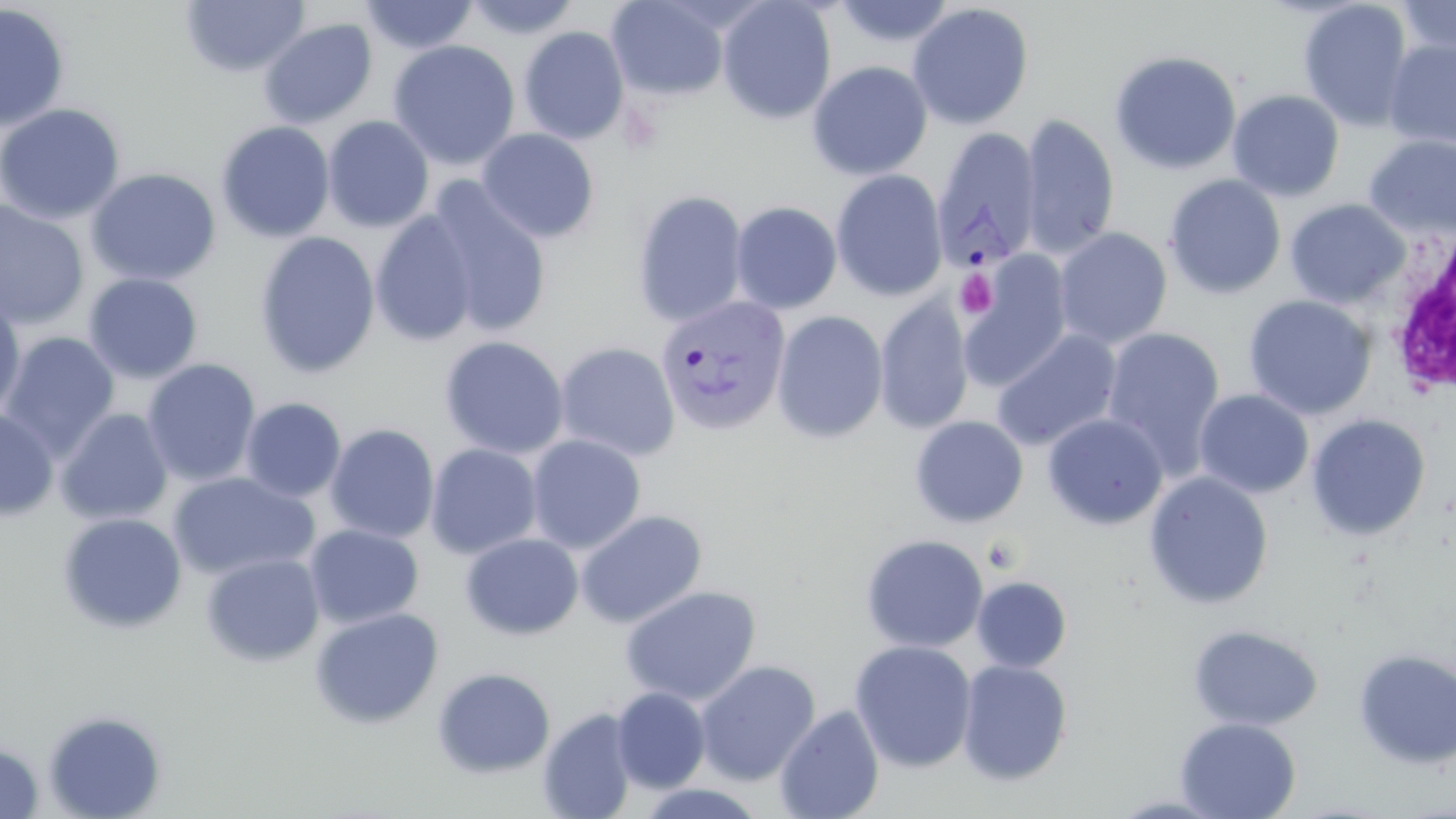

Summary:
  - Coordinate format: approximate bounding boxes as named x1/y1/x2/y2 corners in pixels
  - Platelet locations: (x1=954, y1=269, x2=998, y2=317)
  - White blood cell locations: (x1=1381, y1=218, x2=1456, y2=399)
  - Uninfected red blood cell locations: (x1=180, y1=0, x2=310, y2=78), (x1=359, y1=0, x2=480, y2=55), (x1=463, y1=0, x2=582, y2=40), (x1=606, y1=0, x2=730, y2=102), (x1=716, y1=0, x2=837, y2=124), (x1=833, y1=0, x2=956, y2=48), (x1=1297, y1=0, x2=1415, y2=132), (x1=1396, y1=0, x2=1456, y2=59), (x1=907, y1=3, x2=1034, y2=130), (x1=0, y1=4, x2=71, y2=132), (x1=257, y1=18, x2=377, y2=129), (x1=518, y1=25, x2=630, y2=145), (x1=387, y1=39, x2=520, y2=170), (x1=1383, y1=39, x2=1456, y2=150), (x1=1109, y1=50, x2=1242, y2=175), (x1=807, y1=61, x2=933, y2=180), (x1=1226, y1=90, x2=1345, y2=202), (x1=0, y1=103, x2=126, y2=224), (x1=1019, y1=114, x2=1120, y2=259), (x1=323, y1=115, x2=434, y2=232), (x1=215, y1=120, x2=336, y2=243), (x1=475, y1=128, x2=600, y2=244), (x1=1363, y1=135, x2=1456, y2=241), (x1=85, y1=168, x2=221, y2=287), (x1=831, y1=169, x2=948, y2=302), (x1=1163, y1=174, x2=1287, y2=300), (x1=421, y1=178, x2=554, y2=339), (x1=632, y1=190, x2=749, y2=327), (x1=1285, y1=198, x2=1410, y2=310), (x1=0, y1=199, x2=90, y2=330), (x1=730, y1=201, x2=842, y2=314), (x1=370, y1=211, x2=480, y2=347), (x1=1054, y1=228, x2=1172, y2=349), (x1=254, y1=231, x2=380, y2=378), (x1=959, y1=252, x2=1074, y2=390), (x1=83, y1=273, x2=203, y2=384), (x1=0, y1=294, x2=27, y2=423), (x1=1242, y1=294, x2=1377, y2=421), (x1=874, y1=296, x2=974, y2=435), (x1=772, y1=310, x2=888, y2=443), (x1=1102, y1=327, x2=1226, y2=475), (x1=991, y1=329, x2=1121, y2=451), (x1=1, y1=332, x2=120, y2=460), (x1=439, y1=335, x2=569, y2=459), (x1=555, y1=341, x2=681, y2=462), (x1=141, y1=358, x2=262, y2=487), (x1=1194, y1=388, x2=1314, y2=499), (x1=240, y1=397, x2=346, y2=502), (x1=55, y1=407, x2=174, y2=526), (x1=0, y1=408, x2=59, y2=521), (x1=1042, y1=413, x2=1168, y2=530), (x1=1305, y1=414, x2=1431, y2=542), (x1=909, y1=415, x2=1028, y2=528), (x1=325, y1=423, x2=440, y2=543), (x1=526, y1=435, x2=646, y2=553), (x1=425, y1=443, x2=543, y2=559), (x1=1143, y1=471, x2=1274, y2=610), (x1=167, y1=472, x2=319, y2=581), (x1=574, y1=509, x2=707, y2=628), (x1=56, y1=513, x2=188, y2=634), (x1=304, y1=524, x2=424, y2=629), (x1=460, y1=533, x2=584, y2=640), (x1=860, y1=534, x2=989, y2=653), (x1=201, y1=552, x2=325, y2=668), (x1=971, y1=575, x2=1072, y2=672), (x1=620, y1=585, x2=762, y2=706), (x1=309, y1=606, x2=445, y2=729), (x1=1187, y1=623, x2=1324, y2=732), (x1=849, y1=640, x2=977, y2=772), (x1=1352, y1=648, x2=1456, y2=769), (x1=694, y1=659, x2=821, y2=784), (x1=956, y1=659, x2=1073, y2=785), (x1=431, y1=666, x2=556, y2=779), (x1=611, y1=687, x2=710, y2=793), (x1=774, y1=704, x2=885, y2=819), (x1=538, y1=707, x2=638, y2=819), (x1=42, y1=709, x2=168, y2=819), (x1=1174, y1=717, x2=1301, y2=819), (x1=0, y1=741, x2=44, y2=818), (x1=627, y1=781, x2=771, y2=818)
  - Plasmodium vivax-infected red blood cell locations: (x1=931, y1=127, x2=1042, y2=274), (x1=654, y1=294, x2=791, y2=436)
  - Slide-level diagnosis: Plasmodium vivax
  - Modality: optical microscopy
  - Image size: 1456×819 pixels
  - Magnification: 1000x
  - Field of view: one of a larger specimen
  - Preparation: thin blood smear
  - Stain: May-Grünwald-Giemsa